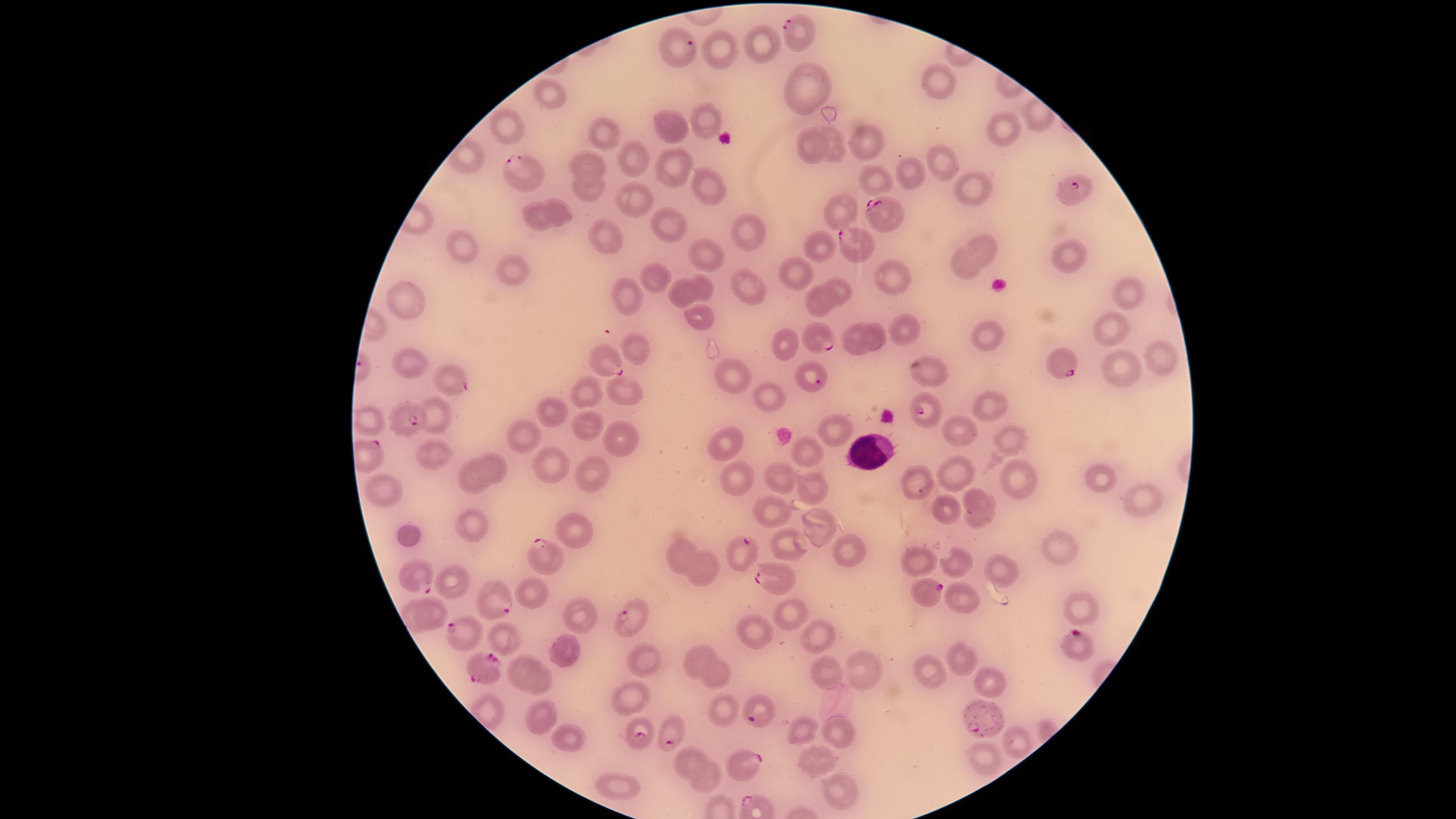
{
  "presence": "malaria parasites seen",
  "visible_region": "circular",
  "uninfected_red_blood_cells": "approximate marker points, in pixels from the top-left corner: (x=761, y=45), (x=723, y=50), (x=937, y=83), (x=800, y=90), (x=549, y=93), (x=704, y=112), (x=509, y=126), (x=672, y=132), (x=1006, y=133), (x=607, y=134), (x=868, y=136), (x=833, y=148), (x=811, y=149), (x=635, y=160), (x=939, y=161), (x=585, y=164), (x=670, y=165), (x=905, y=171), (x=871, y=183), (x=703, y=186), (x=971, y=188), (x=589, y=191), (x=634, y=202), (x=560, y=209), (x=844, y=213), (x=532, y=219), (x=668, y=224), (x=607, y=235), (x=745, y=235), (x=462, y=245), (x=819, y=247), (x=981, y=247), (x=702, y=250), (x=1065, y=257), (x=516, y=271), (x=792, y=272), (x=965, y=273), (x=891, y=275), (x=659, y=279), (x=706, y=286), (x=832, y=286), (x=751, y=288), (x=1123, y=290), (x=683, y=296), (x=628, y=297), (x=408, y=300), (x=814, y=303), (x=701, y=313), (x=1107, y=330), (x=902, y=331), (x=876, y=335), (x=854, y=342), (x=985, y=342), (x=787, y=346), (x=639, y=347), (x=1158, y=360), (x=411, y=365), (x=1124, y=367), (x=931, y=373), (x=731, y=376), (x=589, y=390), (x=620, y=393), (x=769, y=397), (x=997, y=403), (x=550, y=410), (x=586, y=425), (x=832, y=427), (x=959, y=434), (x=522, y=437), (x=725, y=440), (x=1007, y=440), (x=619, y=444), (x=426, y=455), (x=803, y=455), (x=548, y=462), (x=494, y=464), (x=958, y=472), (x=593, y=473), (x=780, y=477), (x=737, y=479), (x=469, y=480), (x=918, y=480), (x=1095, y=480), (x=1017, y=482), (x=810, y=487), (x=385, y=489), (x=1143, y=497), (x=975, y=500), (x=948, y=510), (x=772, y=514), (x=978, y=521), (x=818, y=523), (x=471, y=525), (x=579, y=530), (x=410, y=538), (x=794, y=545), (x=677, y=548), (x=1056, y=548), (x=845, y=549), (x=957, y=562), (x=918, y=563), (x=699, y=570), (x=1004, y=574), (x=456, y=585), (x=528, y=589), (x=962, y=599), (x=1079, y=610), (x=433, y=612), (x=787, y=615), (x=575, y=616), (x=752, y=629), (x=503, y=635), (x=818, y=636), (x=567, y=650), (x=700, y=657), (x=640, y=659), (x=959, y=661), (x=863, y=666), (x=522, y=668), (x=717, y=673), (x=928, y=674), (x=825, y=675), (x=991, y=681), (x=545, y=685), (x=631, y=701), (x=728, y=711), (x=542, y=717), (x=803, y=732), (x=836, y=733), (x=568, y=738), (x=1018, y=740), (x=985, y=759), (x=688, y=760), (x=812, y=760), (x=705, y=778), (x=615, y=786), (x=836, y=789)",
  "capture": "smartphone photograph through the microscope eyepiece",
  "white_blood_cells": "approximate marker points, in pixels from the top-left corner: (x=868, y=447)",
  "image_size": "1456×819 pixels",
  "preparation": "thin smear of blood",
  "parasitized_red_blood_cells": "approximate marker points, in pixels from the top-left corner: (x=799, y=33), (x=676, y=48), (x=524, y=169), (x=1072, y=191), (x=884, y=210), (x=848, y=245), (x=817, y=337), (x=607, y=361), (x=1064, y=363), (x=449, y=375), (x=809, y=379), (x=924, y=410), (x=401, y=423), (x=740, y=551), (x=544, y=558), (x=413, y=575), (x=767, y=579), (x=929, y=592), (x=494, y=607), (x=625, y=618), (x=455, y=628), (x=1077, y=641), (x=484, y=670), (x=761, y=715), (x=985, y=722), (x=636, y=737), (x=671, y=741), (x=750, y=768)",
  "field_of_view": "single",
  "species": "Plasmodium falciparum",
  "stain": "Giemsa"
}